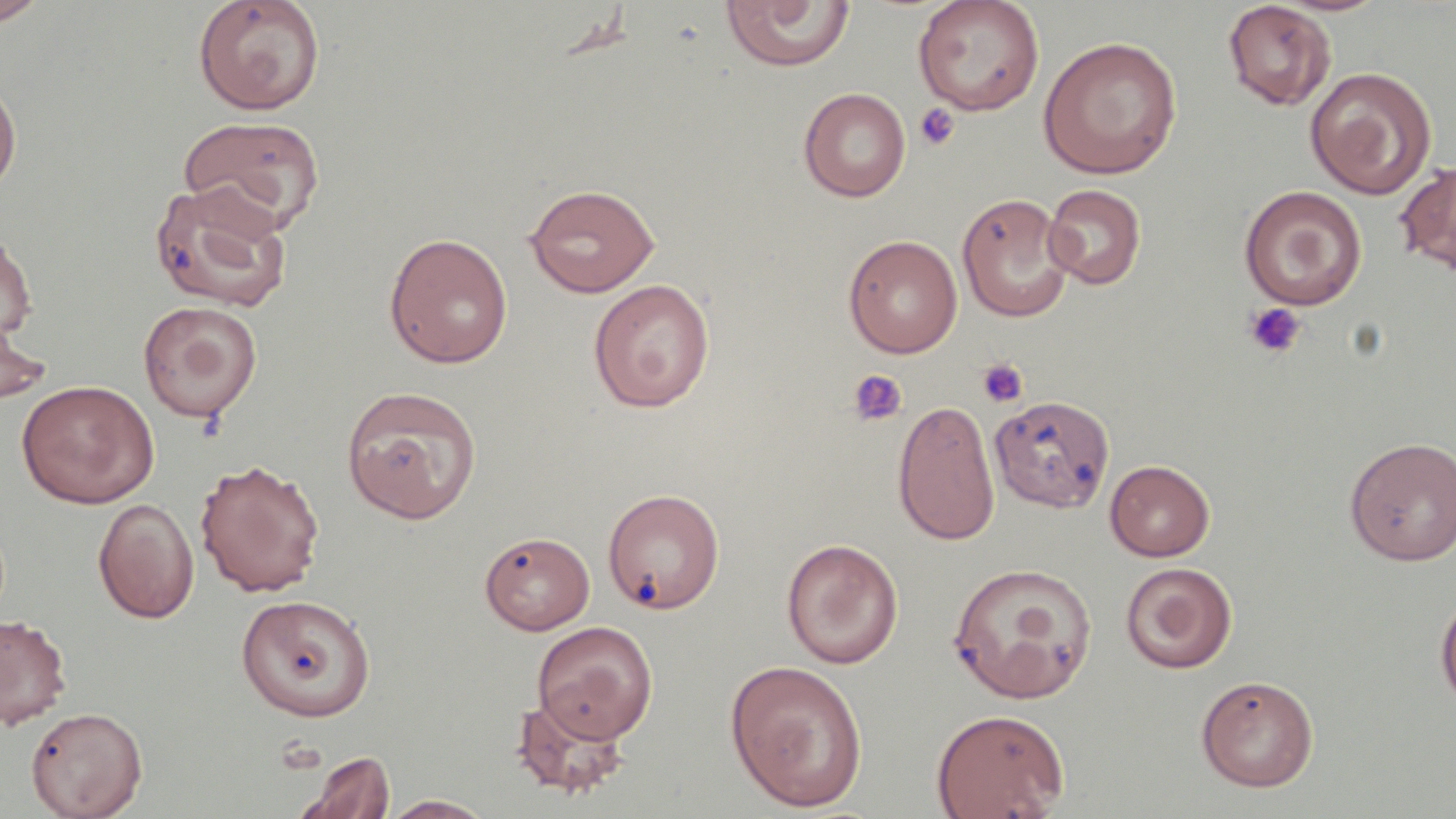

Approximate bounding boxes as (x1, y1, x2, y2) in pixels. Uninfected red blood cell locations: (0, 0, 51, 28), (191, 0, 326, 116), (913, 0, 1045, 116), (720, 1, 854, 72), (1222, 1, 1337, 111), (1038, 36, 1182, 180), (1304, 67, 1437, 199), (0, 74, 22, 200), (798, 87, 911, 202), (177, 116, 328, 236), (1396, 159, 1456, 277), (150, 182, 294, 312), (524, 183, 660, 296), (1043, 184, 1146, 290), (1239, 185, 1367, 310), (957, 192, 1075, 323), (0, 228, 37, 345), (384, 232, 513, 369), (843, 234, 962, 358), (588, 278, 715, 412), (137, 300, 263, 423), (0, 308, 52, 412), (16, 380, 158, 508), (342, 385, 482, 523), (989, 394, 1115, 512), (893, 399, 1000, 545), (1344, 437, 1456, 565), (194, 458, 325, 598), (1105, 460, 1215, 561), (603, 488, 724, 614), (93, 497, 199, 623), (480, 531, 596, 635), (781, 538, 904, 669), (947, 562, 1097, 703), (1120, 562, 1237, 673), (1435, 591, 1456, 711), (235, 594, 376, 722), (0, 614, 72, 729), (532, 621, 657, 743), (724, 659, 868, 811), (1196, 675, 1318, 792), (511, 693, 630, 800), (25, 706, 147, 819), (930, 708, 1070, 819), (294, 750, 397, 819), (381, 794, 495, 818). Platelet locations: (913, 103, 960, 151), (1243, 302, 1306, 359), (977, 358, 1028, 408), (848, 369, 907, 426). Slide-level diagnosis: no evidence of blood parasites. Thin blood film. Image is 1456×819 pixels. Captured at 1000x magnification. May-Grünwald-Giemsa-stained preparation. Light microscopy. Single field of view.